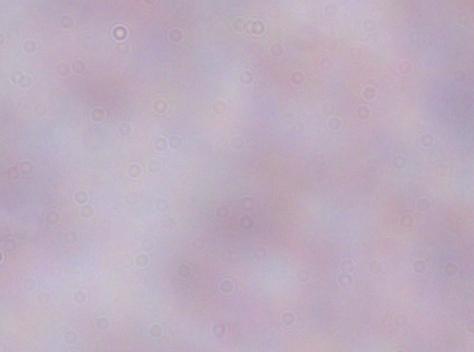

{
  "modality": "photomicrograph",
  "identification": "trypanosome",
  "magnification": "1000x"
}